Identify the parasite.
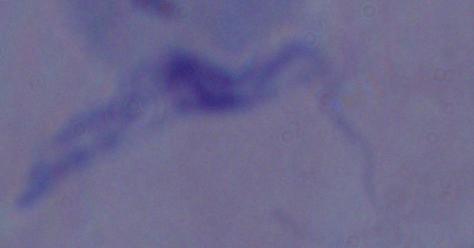
A trypanosome.

Summary:
  - Modality: micrograph
  - Magnification: 1000x